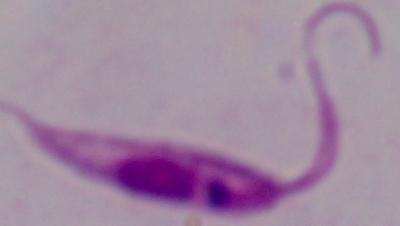
Summary:
  - Identification: Leishmania
  - Magnification: 1000x
  - Modality: micrograph